Assess this cell for malaria.
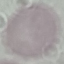

Uninfected.

Thin smear of blood. Photographed with a smartphone camera at the microscope eyepiece. Automatically extracted cell patch, resized to 64 × 64 pixels. Giemsa stain.